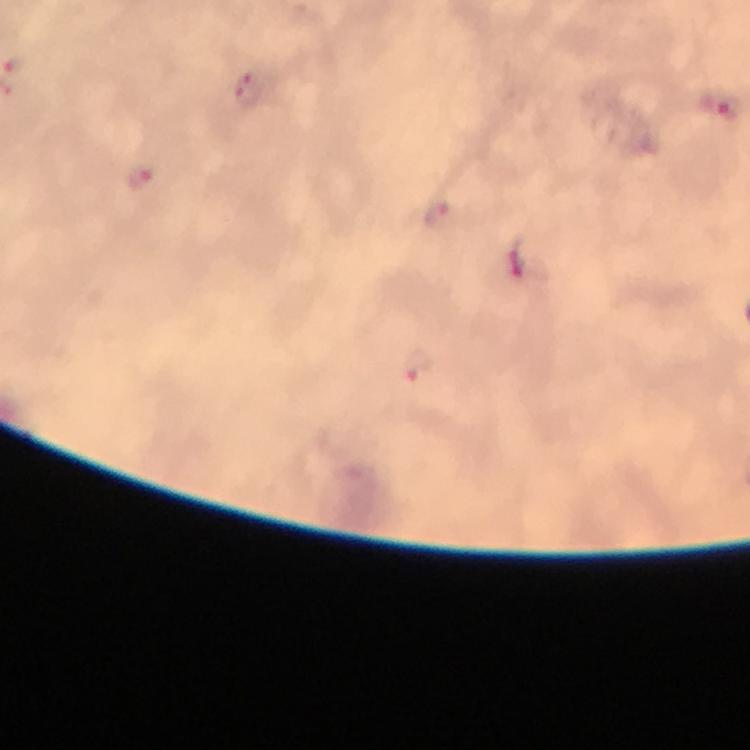 Approximate centers as {x, y} in pixels. Plasmodium parasite locations: {14, 64}, {247, 89}, {719, 106}, {136, 177}, {437, 214}, {517, 265}, {420, 367}. Photographed through the microscope with a smartphone camera. Thick blood smear. Image is 750×750 pixels. Immersion oil was used. Giemsa-stained preparation. 100x magnification. A crop from one field of view. From a malaria diagnostic workup.